Report the malaria status of this cell.
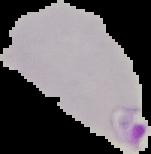
Parasitized.

Summary:
  - Image size: 151×154 pixels
  - Image type: segmented cell region on a black background
  - Preparation: thin blood film